Comment on the morphology of the erythrocytes.
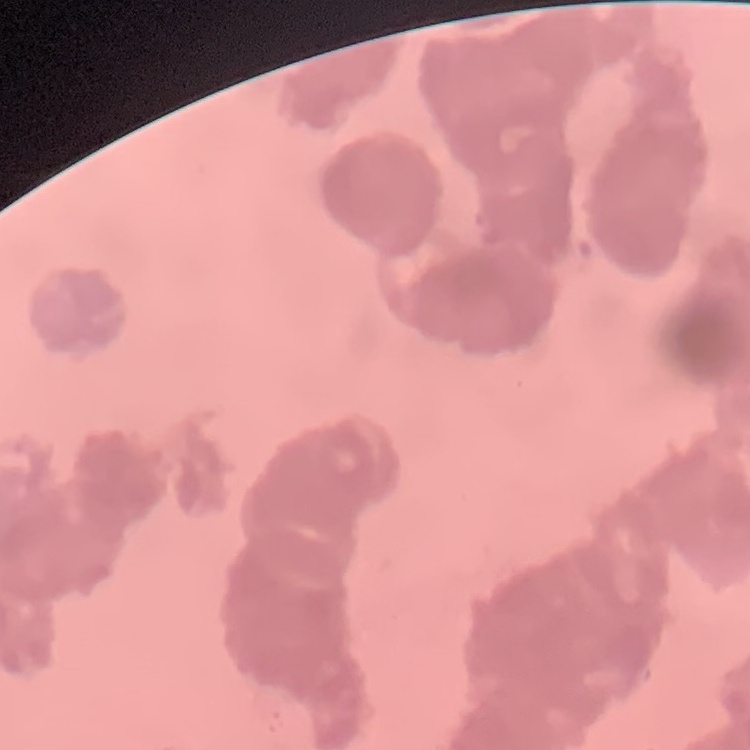

They show rouleaux formation.

Summary:
  - Preparation: thin blood smear
  - Image type: square crop of a larger photomicrograph
  - Stain: Field's or Giemsa